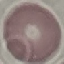

result = no malaria parasites detected
capture = smartphone camera at the microscope eyepiece
stain = Giemsa
preparation = thin blood smear
image type = cell patch, automatically extracted from a larger field of view and resized to 64 × 64 pixels